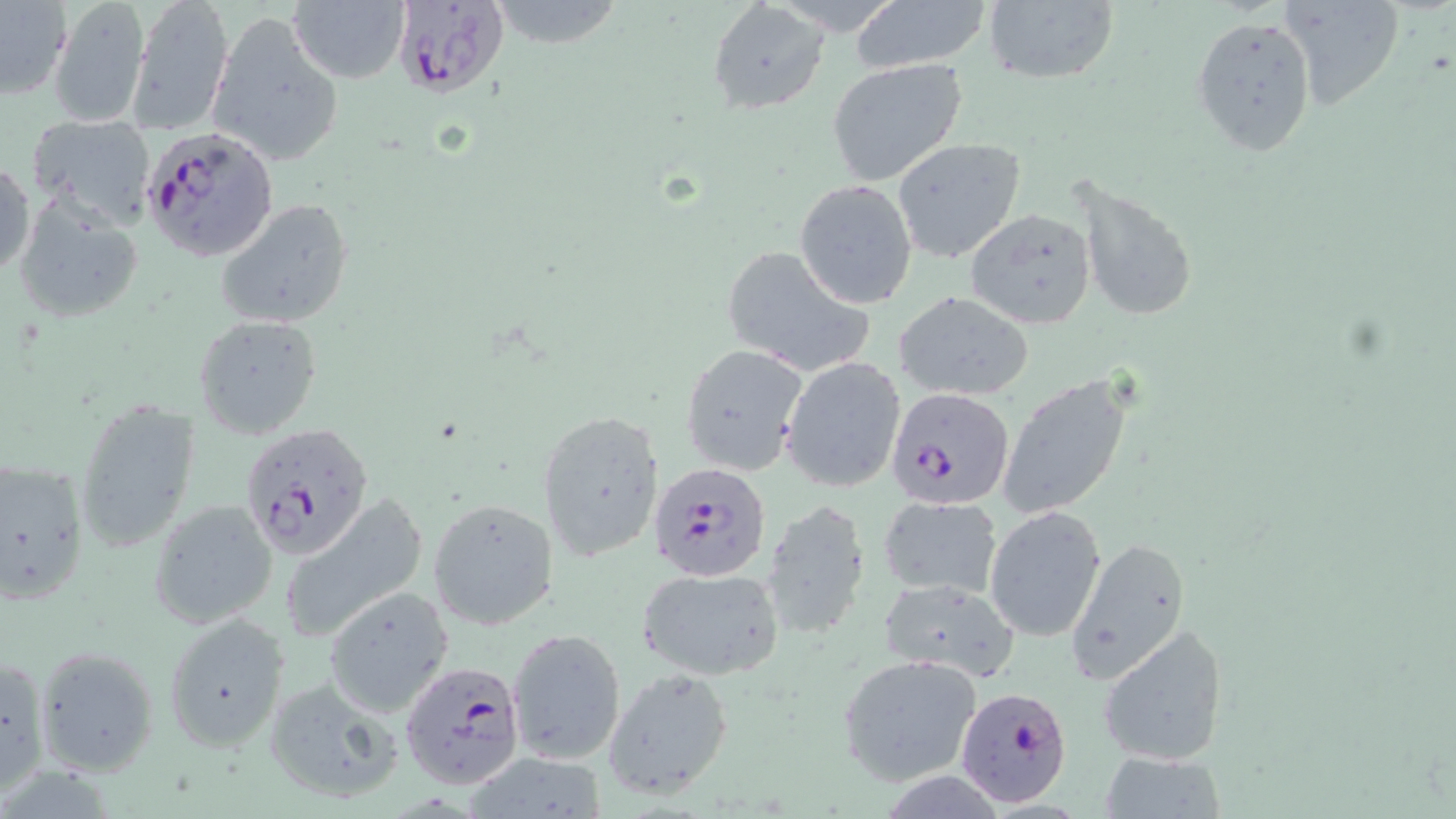

Summary:
  - Coordinate format: approximate bounding boxes as [x1, y1, x2, y2] in pixels
  - Uninfected red blood cell locations: [125, 0, 235, 138], [483, 0, 633, 52], [1275, 0, 1404, 110], [288, 1, 409, 83], [850, 1, 992, 73], [0, 2, 72, 99], [47, 2, 151, 128], [707, 2, 829, 115], [979, 2, 1120, 86], [207, 12, 343, 168], [1192, 14, 1317, 156], [827, 58, 968, 184], [28, 112, 155, 225], [890, 137, 1027, 263], [0, 157, 36, 280], [1071, 173, 1201, 327], [795, 180, 918, 309], [11, 192, 146, 326], [213, 198, 355, 331], [964, 208, 1096, 330], [719, 244, 873, 378], [896, 291, 1035, 401], [194, 315, 323, 439], [681, 343, 809, 476], [780, 357, 907, 493], [998, 377, 1133, 521], [74, 399, 201, 551], [537, 408, 665, 564], [0, 455, 90, 605], [878, 494, 1002, 601], [279, 495, 431, 645], [429, 497, 559, 631], [147, 500, 279, 630], [760, 500, 872, 643], [985, 505, 1106, 640], [1064, 534, 1192, 687], [636, 565, 785, 680], [879, 576, 1022, 681], [323, 585, 456, 717], [163, 613, 290, 752], [1098, 622, 1228, 767], [507, 627, 626, 764], [33, 646, 157, 777], [0, 652, 50, 798], [838, 653, 983, 786], [602, 667, 735, 799], [261, 675, 408, 805], [462, 751, 608, 819], [1097, 752, 1227, 819]
  - Plasmodium falciparum-infected red blood cell locations: [391, 0, 509, 99], [140, 125, 278, 266], [888, 387, 1015, 508], [236, 428, 365, 560], [648, 462, 775, 583], [399, 658, 525, 790], [955, 685, 1074, 808]
  - Slide-level diagnosis: Plasmodium falciparum
  - Field of view: single
  - Magnification: 1000x
  - Modality: light microscopy
  - Stain: May-Grünwald-Giemsa
  - Image size: 1456×819 pixels
  - Preparation: thin blood smear